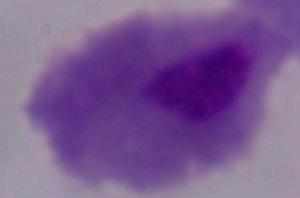

magnification = 1000x
modality = photomicrograph
identification = trichomonad